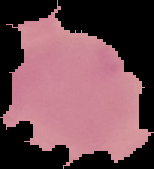
Summary:
  - Preparation: thin blood smear
  - Malaria status: uninfected
  - Image size: 154×169 pixels
  - Image type: segmented cell region with the area outside set to black